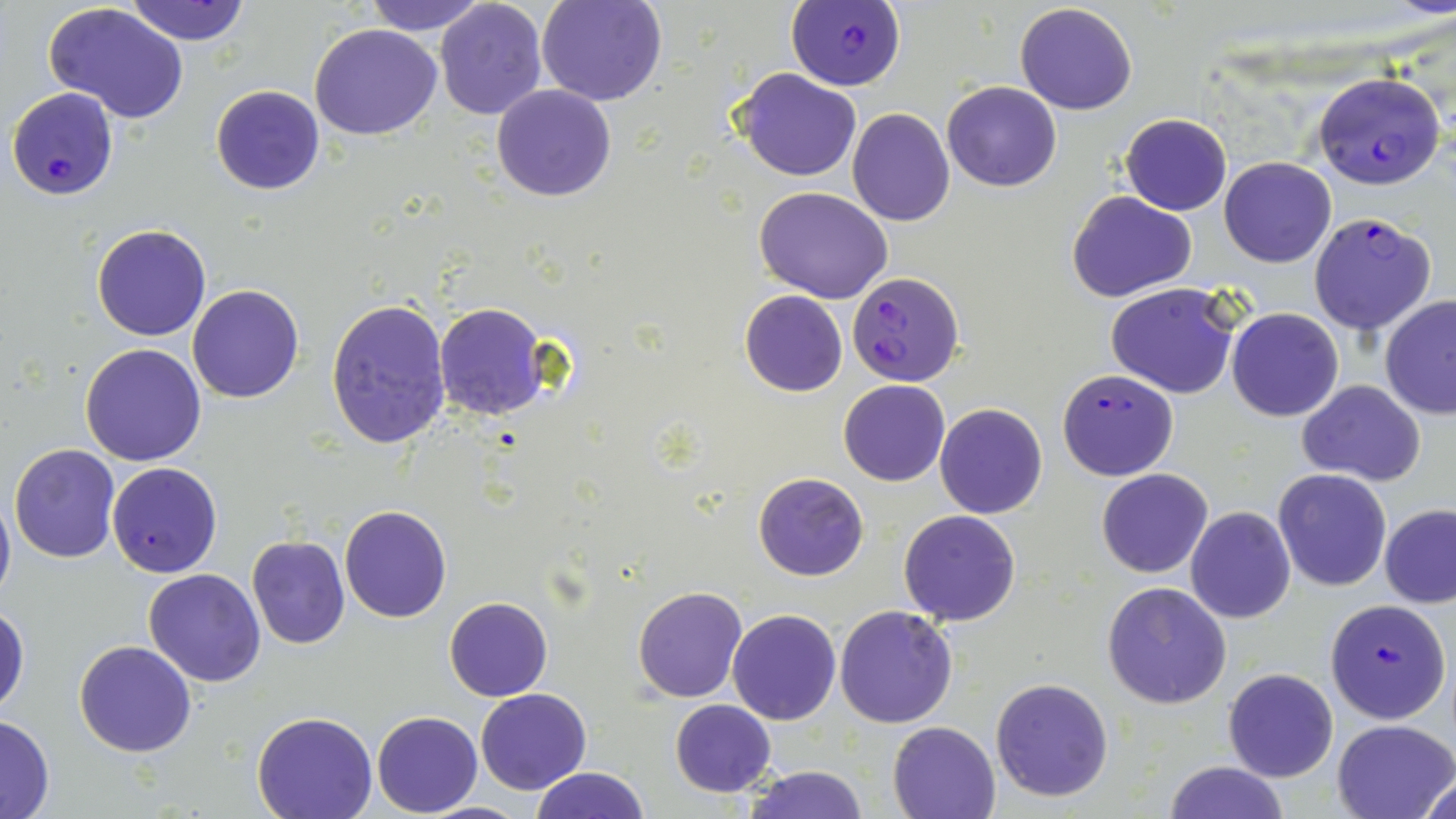

slide-level diagnosis = Plasmodium falciparum
image size = 1456×819 pixels
modality = optical microscopy
uninfected red blood cell locations = approximate bounding boxes as (x1,y1)-(x2,y2) corner pairs in pixels: (125,0)-(253,46), (364,0)-(485,35), (434,0)-(549,121), (538,0)-(667,105), (1015,3)-(1138,115), (44,4)-(190,127), (309,24)-(443,141), (733,68)-(862,182), (942,80)-(1062,193), (491,84)-(618,202), (210,85)-(326,195), (847,109)-(956,227), (1120,112)-(1232,215), (1088,116)-(1219,292), (1219,156)-(1337,267), (754,186)-(893,304), (1067,190)-(1197,302), (92,223)-(211,341), (1105,282)-(1242,399), (187,284)-(305,403), (739,290)-(849,396), (1379,295)-(1456,419), (327,299)-(452,450), (435,303)-(551,420), (1227,308)-(1343,421), (79,344)-(206,466), (838,379)-(950,487), (1297,381)-(1424,485), (935,403)-(1048,518), (9,444)-(122,563), (107,462)-(222,577), (1096,468)-(1213,577), (1272,469)-(1394,592), (754,472)-(868,580), (0,490)-(15,608), (339,506)-(452,622), (1187,507)-(1296,624), (1379,507)-(1456,606), (899,510)-(1020,626), (246,536)-(350,652), (143,568)-(266,686), (1102,582)-(1232,709), (632,586)-(747,703), (444,596)-(552,702), (0,600)-(30,716), (833,605)-(958,729), (727,609)-(841,724), (75,639)-(196,757), (1223,667)-(1339,782), (990,677)-(1114,803), (476,688)-(591,795), (670,700)-(777,797), (252,711)-(379,819), (372,711)-(481,816), (0,713)-(56,819), (1332,719)-(1456,818), (887,720)-(1000,818), (1162,760)-(1290,819), (741,764)-(871,819), (530,767)-(649,819), (1416,769)-(1454,819)
field of view = single
magnification = 1000x
preparation = thin blood smear
Plasmodium falciparum-infected red blood cell locations = approximate bounding boxes as (x1,y1)-(x2,y2) corner pairs in pixels: (788,0)-(904,91), (1311,72)-(1446,190), (7,88)-(119,200), (1310,212)-(1435,336), (847,272)-(963,386), (1057,369)-(1180,481), (1326,600)-(1451,722)
stain = May-Grünwald-Giemsa